Comment on the morphology of the red blood cells.
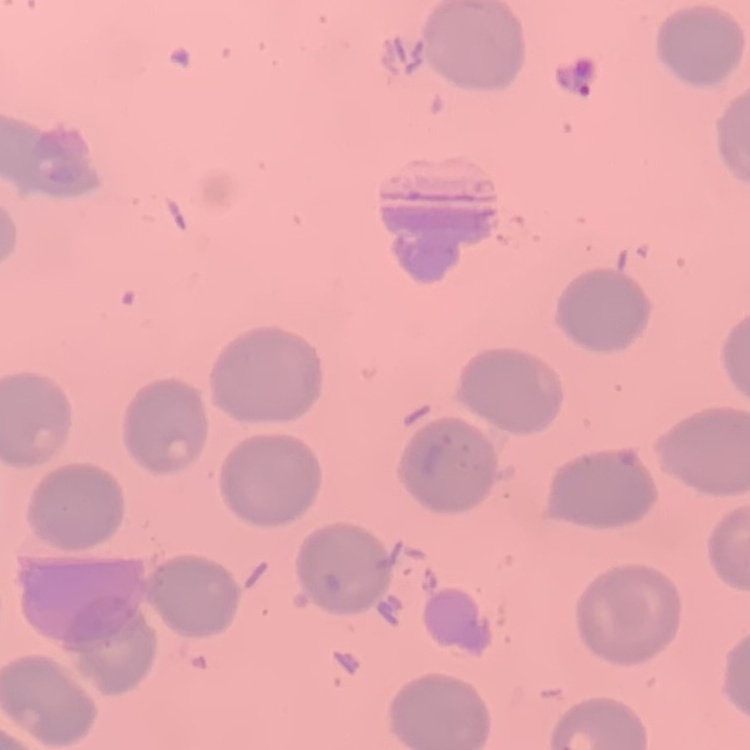

They show no rouleaux formation.

One tile cut from a larger photomicrograph. Field's or Giemsa stain. Thin peripheral smear.